Assess this cell for malaria.
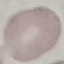
It is uninfected.

Giemsa stain. Thin blood smear. Cell patch, automatically extracted from a larger field of view and resized to 64 × 64 pixels. Acquired by smartphone through the microscope eyepiece.